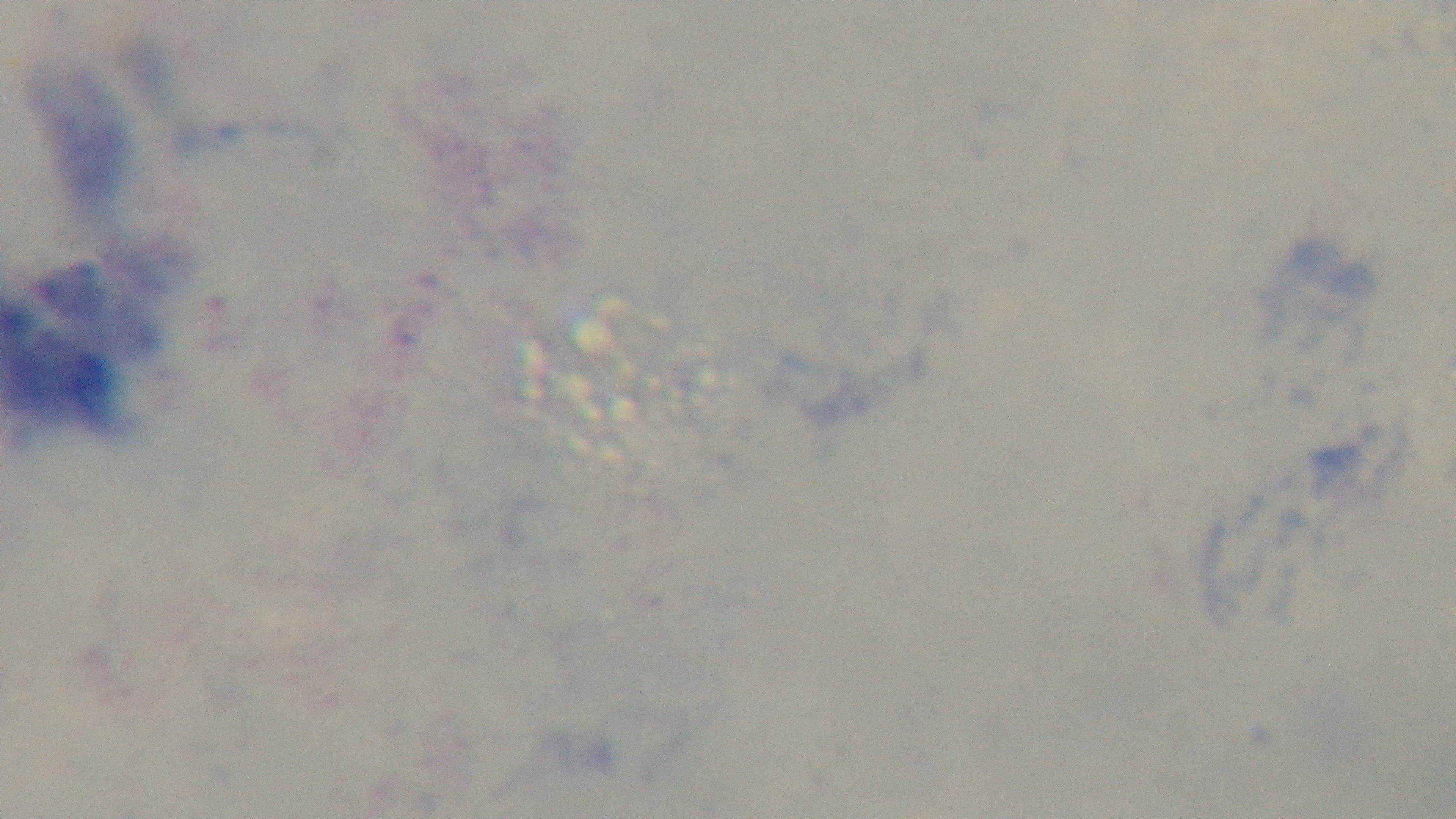
field of view = single
modality = light microscopy
stain = Giemsa
objective = 100x oil immersion
malaria status = uninfected
preparation = thick smear
capture = mounted 4K digital camera